Classify this cell by malaria status.
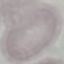
Uninfected.

stain = Giemsa
capture = smartphone camera at the microscope eyepiece
preparation = thin smear
image type = cell patch, automatically extracted from a larger field of view and resized to 64 × 64 pixels